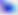
Micrograph. Toxoplasma gondii is seen. 400x magnification.